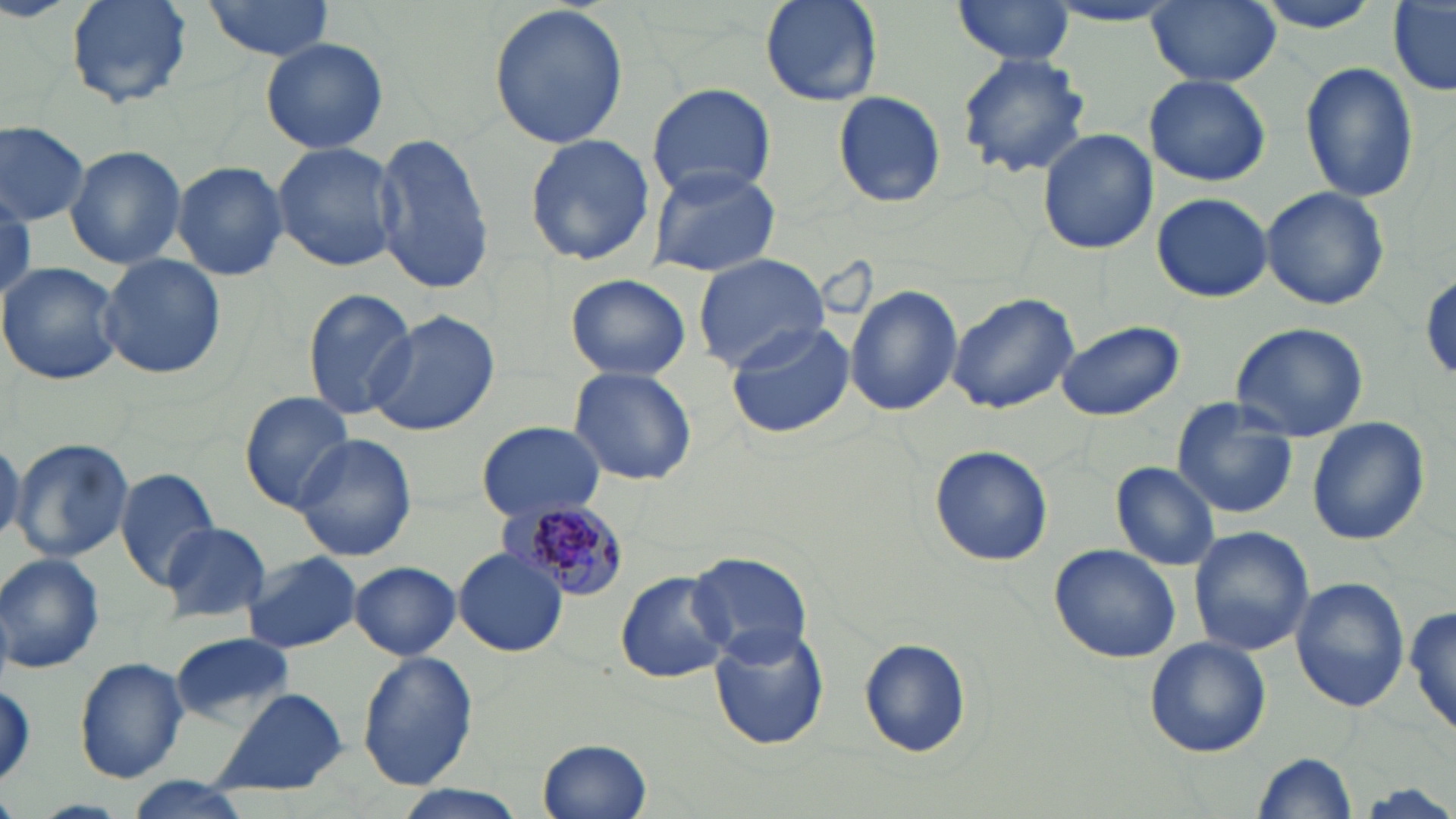
slide_level_diagnosis: Plasmodium malariae
uninfected_red_blood_cell_locations: 'approximate bounding boxes as (x1,y1)-(x2,y2) corner pairs in pixels: (64,0)-(195,108), (760,0)-(883,107), (952,0)-(1078,66), (1143,0)-(1281,88), (1249,0)-(1393,34), (200,1)-(337,59), (1389,1)-(1456,97), (486,4)-(629,150), (1041,4)-(1186,29), (261,35)-(387,154), (955,53)-(1093,177), (1298,61)-(1421,202), (1143,73)-(1272,188), (647,82)-(775,202), (834,92)-(949,207), (0,121)-(88,224), (1037,128)-(1158,255), (370,130)-(494,295), (523,132)-(657,268), (272,141)-(402,272), (65,144)-(187,269), (172,161)-(289,281), (649,167)-(780,277), (1261,186)-(1390,311), (1151,192)-(1272,303), (693,252)-(832,372), (99,253)-(225,380), (0,263)-(123,386), (1422,268)-(1456,384), (565,273)-(690,383), (844,283)-(963,416), (302,286)-(414,421), (947,291)-(1080,414), (362,310)-(503,438), (725,319)-(859,439), (1054,320)-(1183,423), (1229,321)-(1368,442), (568,366)-(697,486), (240,392)-(355,510), (1171,398)-(1299,519), (1306,417)-(1431,546), (478,421)-(604,523), (291,432)-(418,562), (0,433)-(23,551), (10,437)-(136,565), (929,445)-(1054,567), (1110,462)-(1221,572), (114,468)-(222,588), (163,519)-(271,623), (1188,527)-(1314,657), (1049,543)-(1182,664), (452,547)-(569,656), (688,549)-(812,663), (241,551)-(362,654), (0,553)-(107,674), (349,561)-(461,659), (616,571)-(732,684), (1290,577)-(1411,711), (1407,602)-(1456,741), (709,624)-(830,750), (171,633)-(294,727), (1143,637)-(1271,758), (858,639)-(972,758), (355,653)-(479,789), (75,657)-(189,782), (210,690)-(349,798), (536,737)-(651,817), (1252,753)-(1358,817), (127,777)-(258,818)'
preparation: thin blood film
magnification: 1000x
field_of_view: one of a larger specimen
modality: optical microscopy
image_size: 1456×819 pixels
stain: May-Grünwald-Giemsa
plasmodium_malariae_infected_red_blood_cell_locations: 'approximate bounding boxes as (x1,y1)-(x2,y2) corner pairs in pixels: (514,500)-(631,603)'